Assess this cell for malaria.
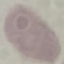
It is uninfected.

Summary:
  - Image type: cell patch, automatically extracted from a larger field of view and resized to 64 × 64 pixels
  - Capture: smartphone through the microscope eyepiece
  - Stain: Giemsa
  - Preparation: thin smear